Name the blood parasite species.
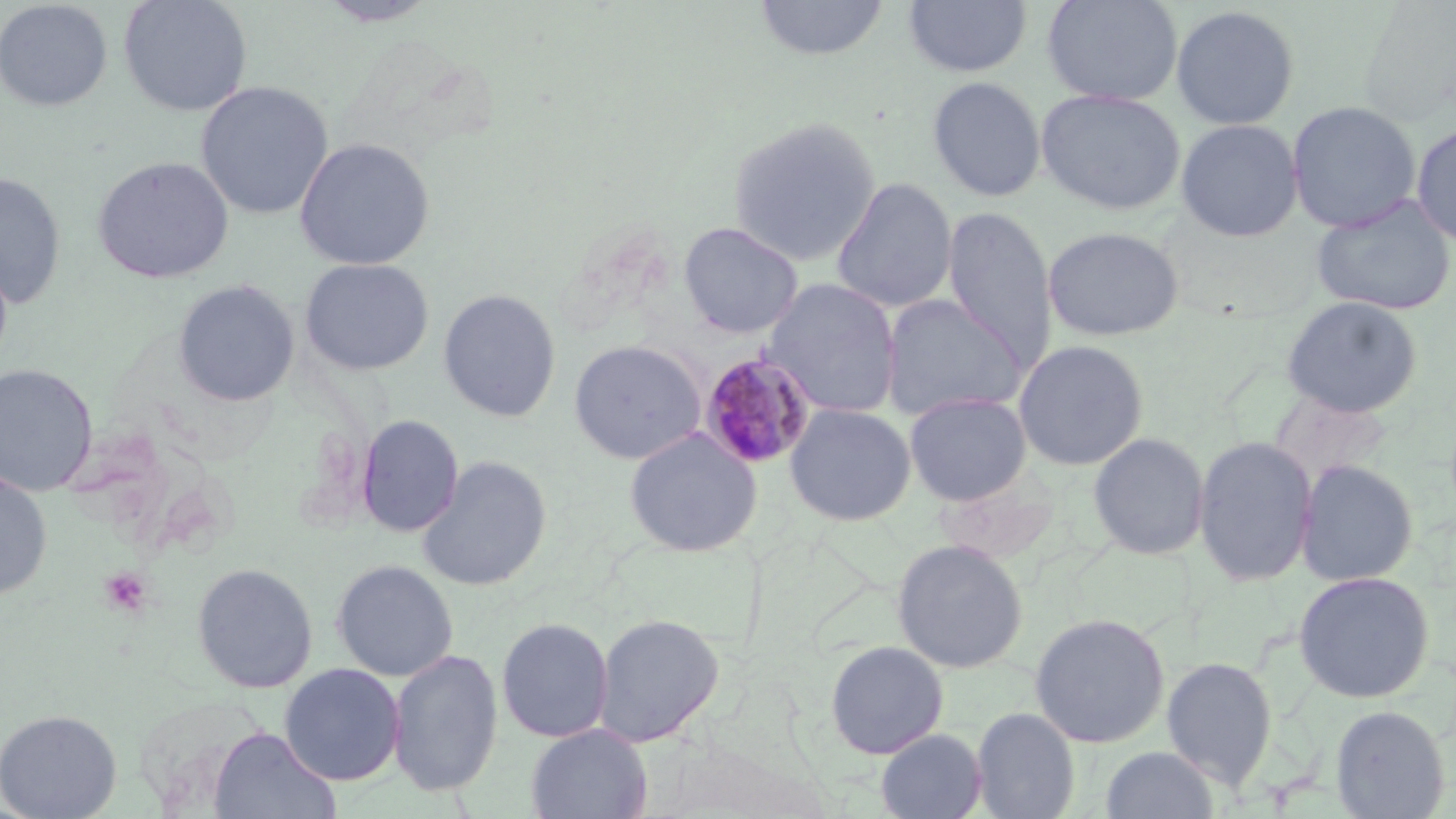
Plasmodium malariae.

Approximate bounding boxes as (x1,y1)-(x2,y2) corner pairs in pixels. Platelet locations: (99,567)-(152,618). Uninfected red blood cell locations: (0,0)-(113,112), (118,0)-(253,117), (754,0)-(890,61), (904,0)-(1032,77), (1042,0)-(1184,106), (317,1)-(441,26), (1170,5)-(1300,130), (927,76)-(1047,202), (196,81)-(333,220), (1036,88)-(1186,215), (1287,101)-(1421,234), (727,116)-(882,267), (1176,119)-(1303,242), (1411,121)-(1456,248), (294,137)-(435,271), (92,156)-(234,283), (0,172)-(66,309), (831,177)-(957,314), (1310,194)-(1456,317), (943,206)-(1057,373), (678,221)-(804,339), (1042,225)-(1184,342), (299,257)-(434,376), (762,277)-(902,417), (173,279)-(300,407), (439,289)-(561,422), (879,293)-(1027,422), (1281,296)-(1423,418), (569,339)-(706,464), (1013,339)-(1149,471), (0,364)-(98,496), (904,392)-(1032,505), (784,403)-(916,526), (356,414)-(464,537), (624,428)-(761,557), (1087,432)-(1210,560), (1193,435)-(1318,587), (417,455)-(552,591), (1295,458)-(1419,586), (0,468)-(53,602), (891,538)-(1028,674), (332,559)-(458,681), (192,562)-(318,694), (1293,570)-(1436,703), (1029,612)-(1170,749), (594,613)-(725,747), (497,617)-(614,743), (824,640)-(949,759), (388,648)-(503,797), (1161,655)-(1277,790), (279,663)-(405,786), (1330,704)-(1451,818), (971,706)-(1080,819), (0,708)-(122,819), (527,724)-(652,819), (208,726)-(341,819), (876,728)-(988,819), (1100,745)-(1220,819). Plasmodium malariae-infected red blood cell locations: (699,352)-(817,470). Light microscopy. Thin blood film. Single field of view. Captured at 1000x magnification. Image is 1456×819 pixels. May-Grünwald-Giemsa stain.